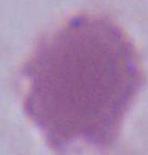

magnification = 1000x
modality = photomicrograph
identification = red blood cell